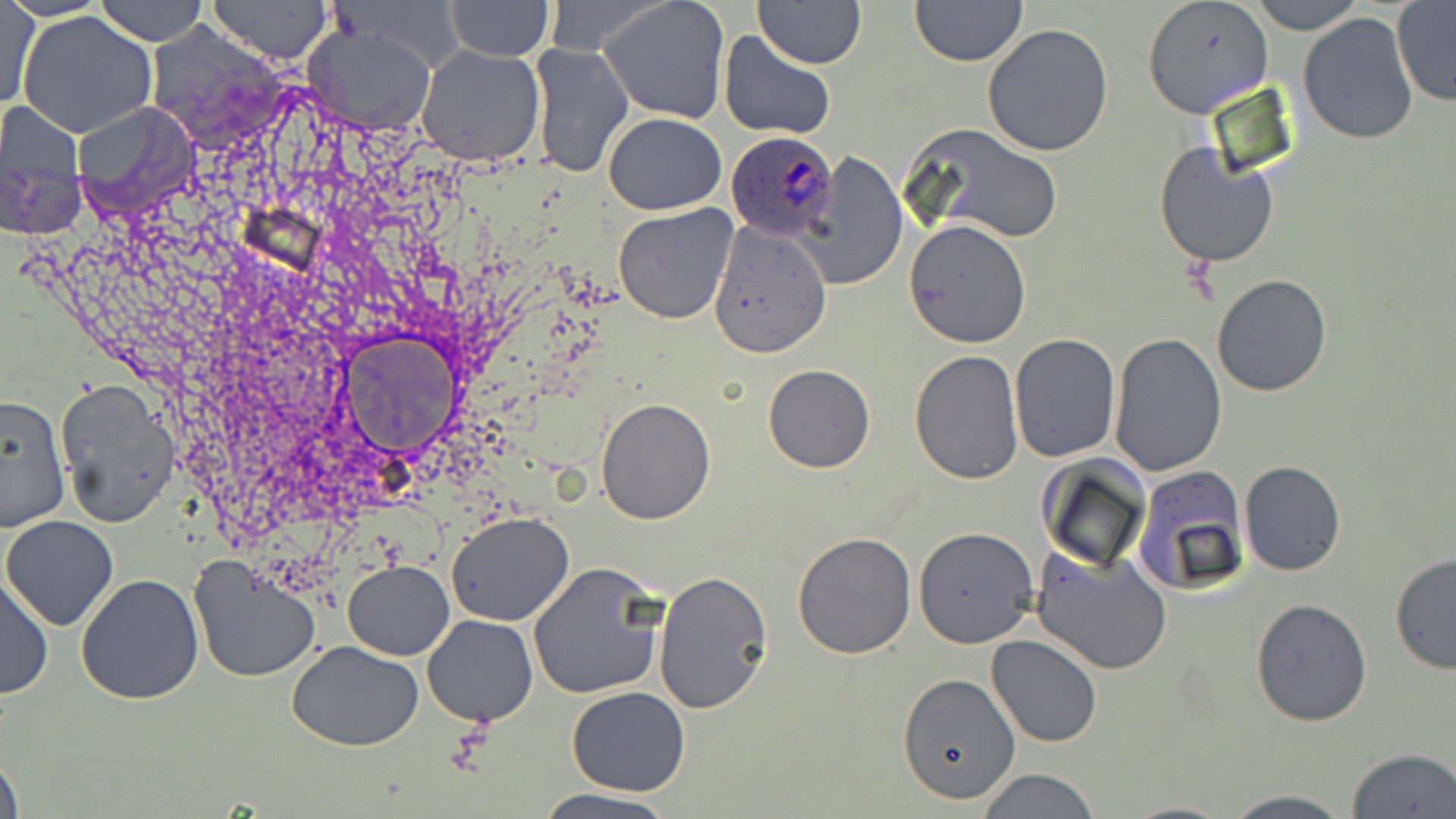
slide_level_diagnosis: Plasmodium ovale
magnification: 1000x
uninfected_red_blood_cell_locations: 'approximate bounding boxes as (x1, y1, x2, y2) in pixels: (95, 0, 209, 46), (207, 0, 331, 65), (598, 0, 731, 122), (910, 0, 1026, 66), (1142, 0, 1274, 118), (1248, 0, 1363, 31), (445, 1, 552, 62), (1, 2, 37, 110), (754, 2, 866, 68), (1392, 2, 1456, 106), (17, 10, 158, 139), (1296, 12, 1420, 144), (303, 24, 438, 134), (982, 24, 1115, 157), (717, 30, 837, 140), (528, 40, 634, 180), (416, 44, 546, 168), (73, 103, 200, 216), (0, 104, 83, 179), (603, 112, 727, 214), (908, 122, 1065, 246), (1154, 142, 1278, 268), (805, 150, 907, 292), (1, 169, 87, 238), (612, 203, 738, 324), (903, 219, 1032, 348), (709, 220, 832, 357), (1212, 273, 1332, 396), (1109, 332, 1228, 476), (1008, 334, 1119, 462), (909, 349, 1025, 485), (763, 364, 875, 473), (55, 381, 179, 527), (0, 394, 71, 531), (594, 395, 715, 523), (1239, 460, 1345, 575), (1129, 467, 1249, 595), (445, 511, 574, 626), (1, 516, 120, 632), (912, 527, 1038, 646), (792, 531, 919, 660), (1031, 547, 1171, 675), (1389, 552, 1456, 674), (188, 554, 323, 682), (344, 561, 453, 659), (528, 563, 667, 700), (653, 572, 771, 714), (0, 573, 52, 701), (75, 573, 204, 706), (1250, 598, 1372, 727), (423, 615, 537, 726), (987, 634, 1103, 748), (285, 641, 425, 750), (897, 672, 1022, 806), (567, 686, 691, 797), (1344, 748, 1455, 819), (0, 749, 25, 819), (976, 769, 1100, 819), (533, 791, 683, 819), (1220, 791, 1357, 819)'
image_size: 1456×819 pixels
field_of_view: one of a larger specimen
plasmodium_ovale_infected_red_blood_cell_locations: 'approximate bounding boxes as (x1, y1, x2, y2) in pixels: (725, 130, 842, 241)'
modality: optical microscopy
stain: May-Grünwald-Giemsa
preparation: thin blood smear